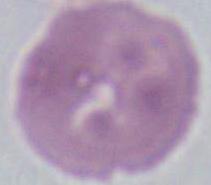
Summary:
  - Modality: photomicrograph
  - Magnification: 1000x
  - Identification: red blood cell